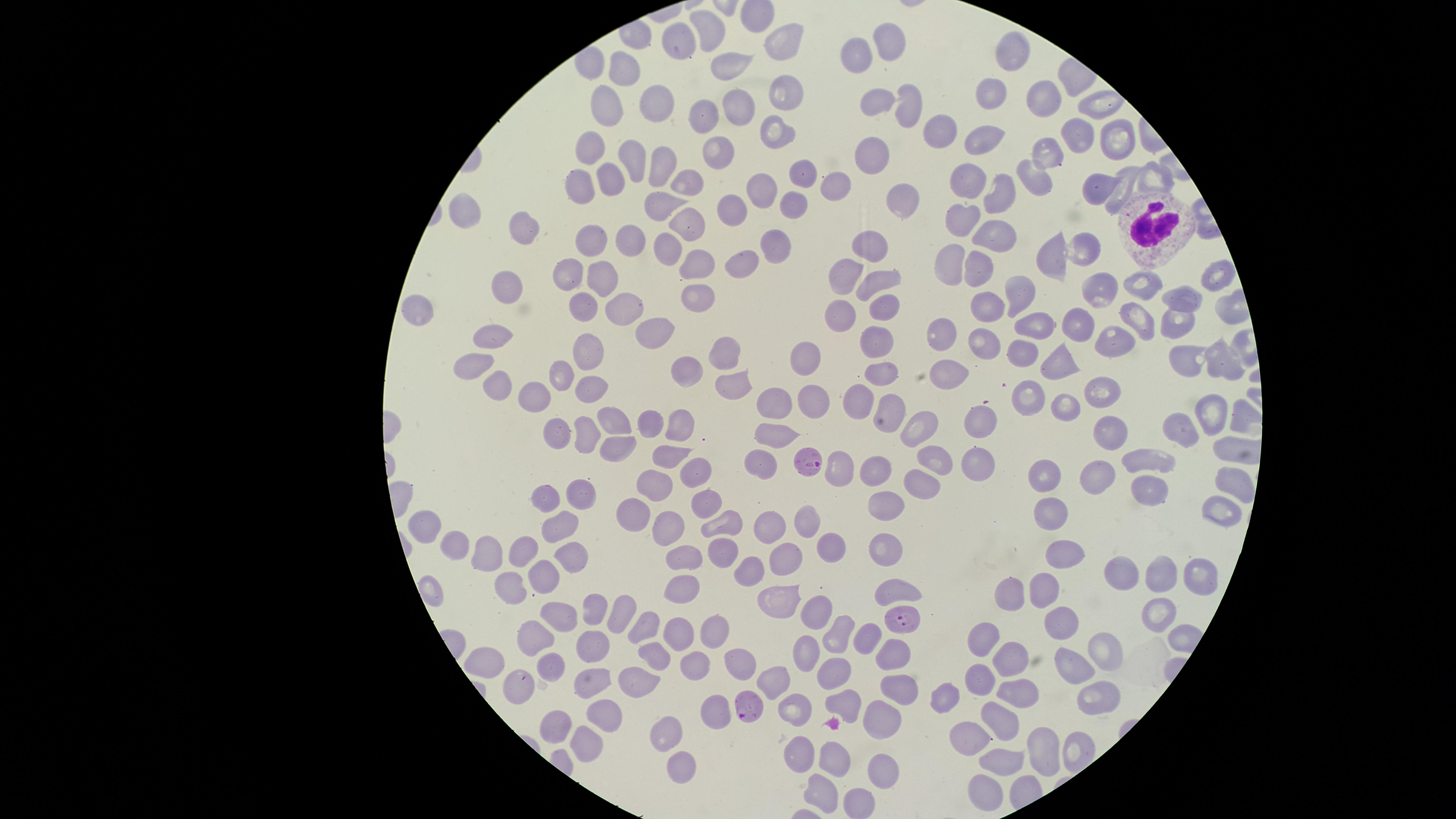
Approximate marker points as (x, y) in pixels. Uninfected RBCs: (707, 30), (890, 38), (777, 40), (678, 49), (858, 54), (1011, 55), (729, 66), (628, 73), (786, 91), (874, 95), (992, 95), (656, 102), (1038, 103), (1089, 104), (906, 105), (608, 106), (739, 109), (711, 115), (781, 131), (940, 131), (988, 135), (1069, 138), (1114, 139), (592, 146), (718, 150), (874, 154), (633, 160), (1041, 164), (664, 168), (795, 172), (580, 177), (968, 178), (1149, 178), (612, 179), (1032, 179), (1121, 181), (688, 182), (758, 183), (832, 184), (998, 192), (1092, 192), (902, 193), (659, 200), (787, 210), (730, 211), (466, 212), (684, 218), (966, 224), (520, 228), (996, 232), (874, 240), (630, 243), (593, 244), (772, 244), (670, 249), (1078, 252), (1043, 257), (737, 261), (948, 265), (702, 266), (850, 269), (974, 269), (881, 271), (569, 273), (1213, 278), (601, 280), (1139, 285), (1103, 287), (503, 289), (1013, 289), (694, 297), (1180, 299), (984, 302), (579, 305), (630, 305), (879, 307), (420, 311), (1133, 313), (836, 314), (1171, 318), (1075, 323), (1036, 324), (495, 333), (648, 333), (943, 333), (878, 334), (1109, 340), (984, 345), (724, 348), (1024, 348), (803, 351), (591, 354), (1060, 356), (1220, 357), (1173, 358), (468, 361), (687, 369), (947, 370), (882, 371), (558, 373), (735, 381), (596, 384), (497, 390), (1024, 394), (860, 396), (1097, 396), (534, 398), (815, 398), (772, 401), (1066, 406), (1210, 409), (884, 410), (616, 415), (984, 415), (650, 419), (679, 422), (1184, 425), (919, 428), (1111, 430), (554, 432), (774, 432), (583, 437), (671, 451), (1149, 454), (761, 458), (931, 460), (976, 462), (842, 470), (697, 472), (1102, 472), (876, 473), (1049, 477), (1226, 482), (656, 487), (580, 489), (922, 490), (1148, 491), (549, 495), (704, 497), (876, 501), (1217, 504), (635, 509), (1052, 509), (804, 518), (666, 519), (722, 520), (765, 525), (558, 527), (429, 531), (832, 546), (884, 547), (454, 548), (525, 548), (717, 551), (485, 553), (1066, 553), (684, 555), (781, 555), (572, 556), (1121, 571), (547, 573), (745, 573), (1197, 573), (1157, 575), (514, 582), (894, 584), (680, 585), (1014, 587), (1053, 590), (779, 604), (1157, 609), (592, 612), (562, 616), (622, 616), (1063, 621), (816, 622), (646, 626), (675, 626), (841, 628), (714, 632), (538, 635), (984, 635), (870, 636), (594, 647), (807, 648), (1098, 648), (653, 652), (890, 653), (489, 660), (744, 660), (1011, 662), (698, 663), (1069, 667), (547, 668), (836, 672), (773, 674), (592, 676), (637, 678), (983, 679), (898, 686), (514, 687), (1015, 689), (943, 691), (1096, 694), (848, 705), (793, 709), (605, 710), (715, 710), (882, 717), (556, 719), (998, 725), (666, 728), (974, 741), (581, 742), (1039, 749), (797, 753), (831, 759), (1005, 761), (676, 768), (882, 768), (823, 791), (977, 794), (857, 805). WBCs: (1144, 228). Parasitized RBCs: (811, 460), (909, 618), (751, 706). Presence: malaria parasites detected. Image is 1456×819 pixels. Giemsa-stained preparation. Species: Plasmodium falciparum. Photographed with a smartphone camera through the microscope eyepiece. One field of view of the specimen. Circular visible region. Thin smear of blood.